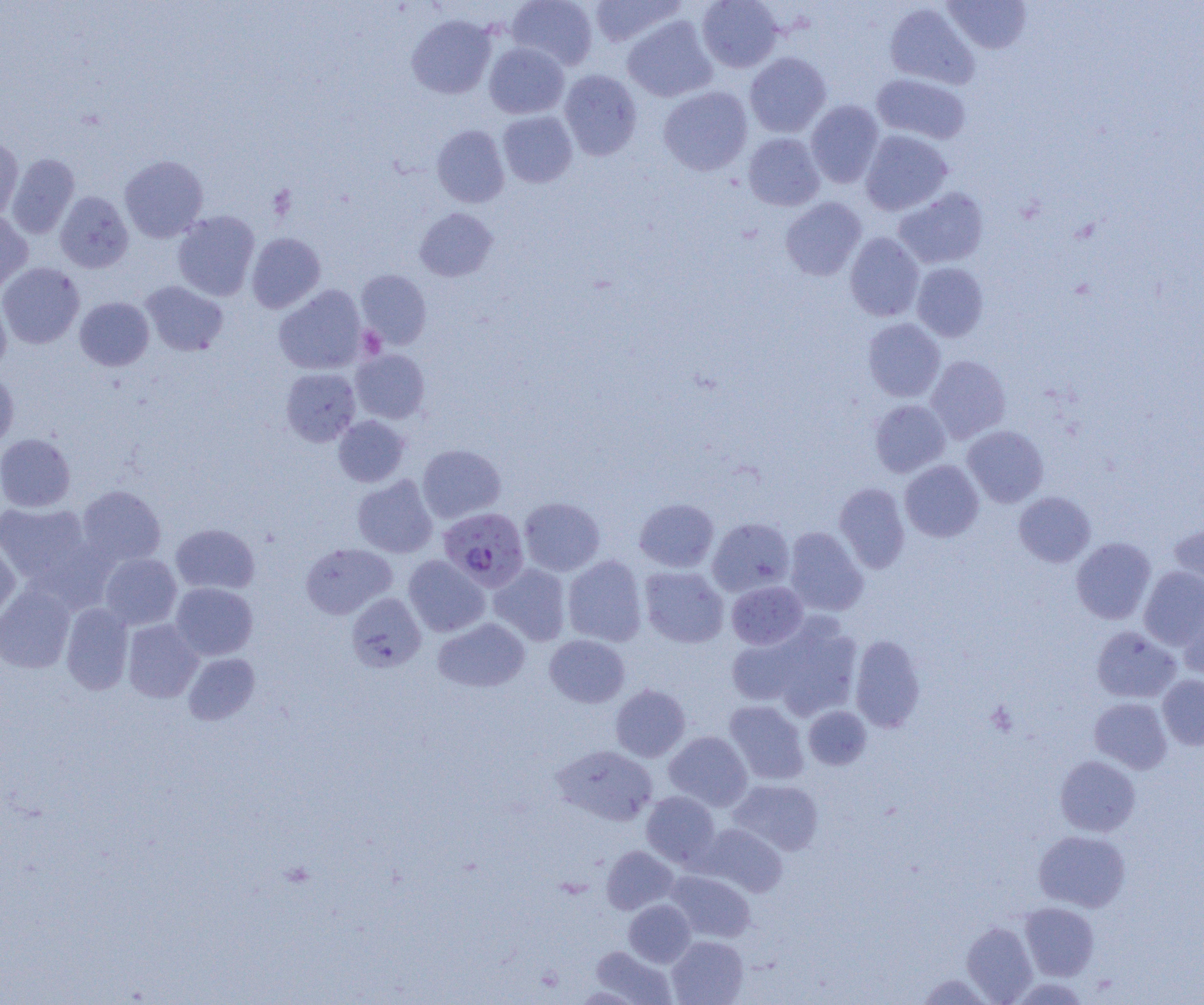

Summary:
  - Coordinate format: approximate bounding boxes as (x1,y1)-(x2,y2) corner pairs in pixels
  - Uninfected red blood cell locations: (507,0)-(598,70), (587,0)-(687,48), (697,0)-(783,72), (943,1)-(1032,53), (884,3)-(980,90), (407,14)-(497,99), (622,15)-(717,102), (484,42)-(569,118), (745,52)-(831,138), (559,70)-(642,160), (871,73)-(970,144), (658,86)-(752,175), (806,100)-(884,187), (498,111)-(577,188), (432,125)-(509,207), (860,130)-(952,215), (743,133)-(825,211), (0,134)-(23,221), (7,153)-(79,239), (119,155)-(208,243), (893,187)-(989,269), (55,191)-(133,272), (780,197)-(866,281), (415,207)-(498,281), (0,210)-(32,293), (172,210)-(259,301), (247,232)-(325,313), (845,232)-(924,321), (0,262)-(84,348), (912,262)-(989,342), (356,269)-(431,348), (141,281)-(228,356), (274,285)-(366,374), (0,295)-(11,373), (75,297)-(154,370), (863,318)-(945,402), (351,349)-(430,423), (925,355)-(1010,443), (280,367)-(360,446), (0,369)-(18,452), (870,399)-(950,477), (333,415)-(410,487), (963,425)-(1048,507), (0,434)-(76,512), (417,444)-(506,522), (900,460)-(984,542), (352,475)-(438,558), (834,482)-(910,573), (77,485)-(166,568), (1013,491)-(1095,567), (519,497)-(605,576), (634,498)-(719,572), (0,502)-(92,585), (707,517)-(795,596), (170,523)-(259,595), (1169,524)-(1204,598), (784,527)-(868,616), (1071,537)-(1156,624), (0,539)-(20,625), (301,543)-(396,619), (99,553)-(182,629), (404,555)-(490,636), (563,555)-(647,647), (488,563)-(571,646), (639,566)-(729,647), (1139,566)-(1204,650), (727,580)-(808,650), (170,583)-(258,660), (0,585)-(75,673), (346,593)-(426,673), (1180,602)-(1204,681), (61,603)-(133,694), (433,618)-(530,692), (123,619)-(203,702), (767,619)-(863,719), (1092,626)-(1181,703), (726,634)-(808,706), (545,635)-(630,707), (850,635)-(925,732), (183,652)-(260,725), (1158,675)-(1204,749), (610,684)-(690,761), (1089,697)-(1172,774), (724,700)-(809,784), (804,706)-(872,769), (664,731)-(752,811), (553,745)-(658,826), (1055,755)-(1140,837), (729,779)-(824,855), (641,791)-(721,867), (698,823)-(787,896), (1033,831)-(1130,912), (602,846)-(678,914), (666,870)-(755,942), (624,900)-(695,967), (1020,902)-(1099,980), (961,921)-(1037,1003), (667,935)-(748,1005), (589,945)-(676,1004), (916,972)-(993,1004)
  - Platelet locations: (357,326)-(385,359)
  - Plasmodium falciparum-infected red blood cell locations: (438,507)-(529,590)
  - Slide-level diagnosis: Plasmodium falciparum
  - Magnification: 1000x
  - Preparation: thin blood smear
  - Image size: 1204×1005 pixels
  - Modality: optical microscopy
  - Field of view: single